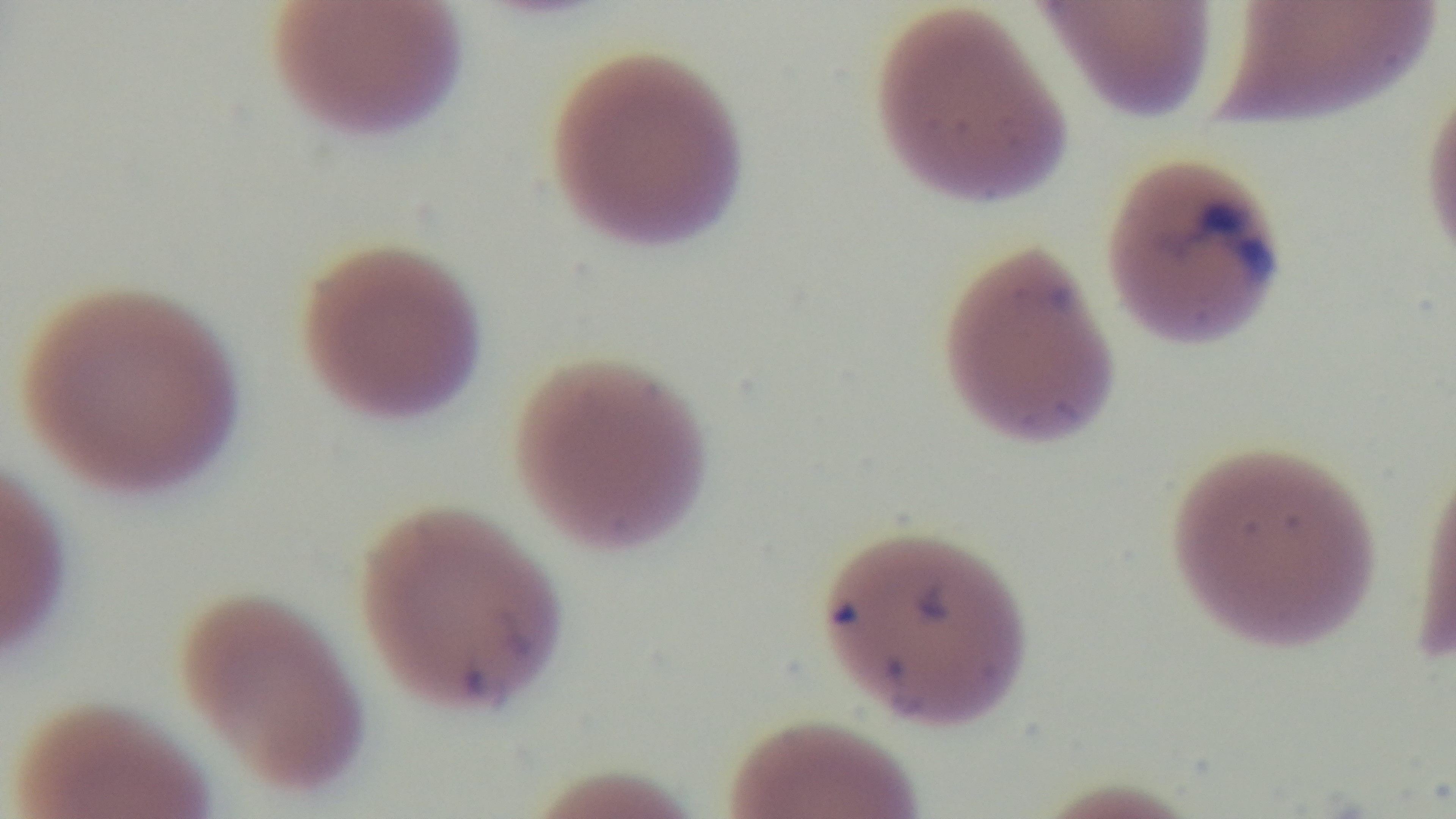

Oil-immersion objective, 100x. Preparation: thin smear. Malaria status: positive. Light microscopy. Giemsa stain. One field from the slide. Captured with a mounted 4K digital camera.